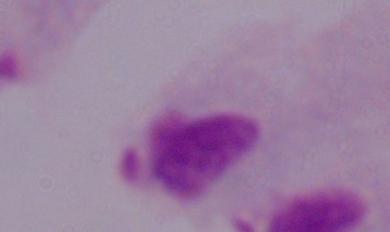
Summary:
  - Identification: trichomonad
  - Modality: photomicrograph
  - Magnification: 1000x